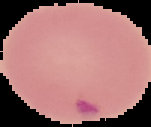

Summary:
  - Preparation: thin blood film
  - Image type: cell region segmented out of the field of view; surrounding area masked to black
  - Image size: 151×127 pixels
  - Malaria status: parasitized